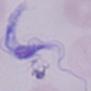
Summary:
  - Modality: micrograph
  - Magnification: 1000x
  - Identification: trypanosome